Locate every Plasmodium parasite and every leukocyte.
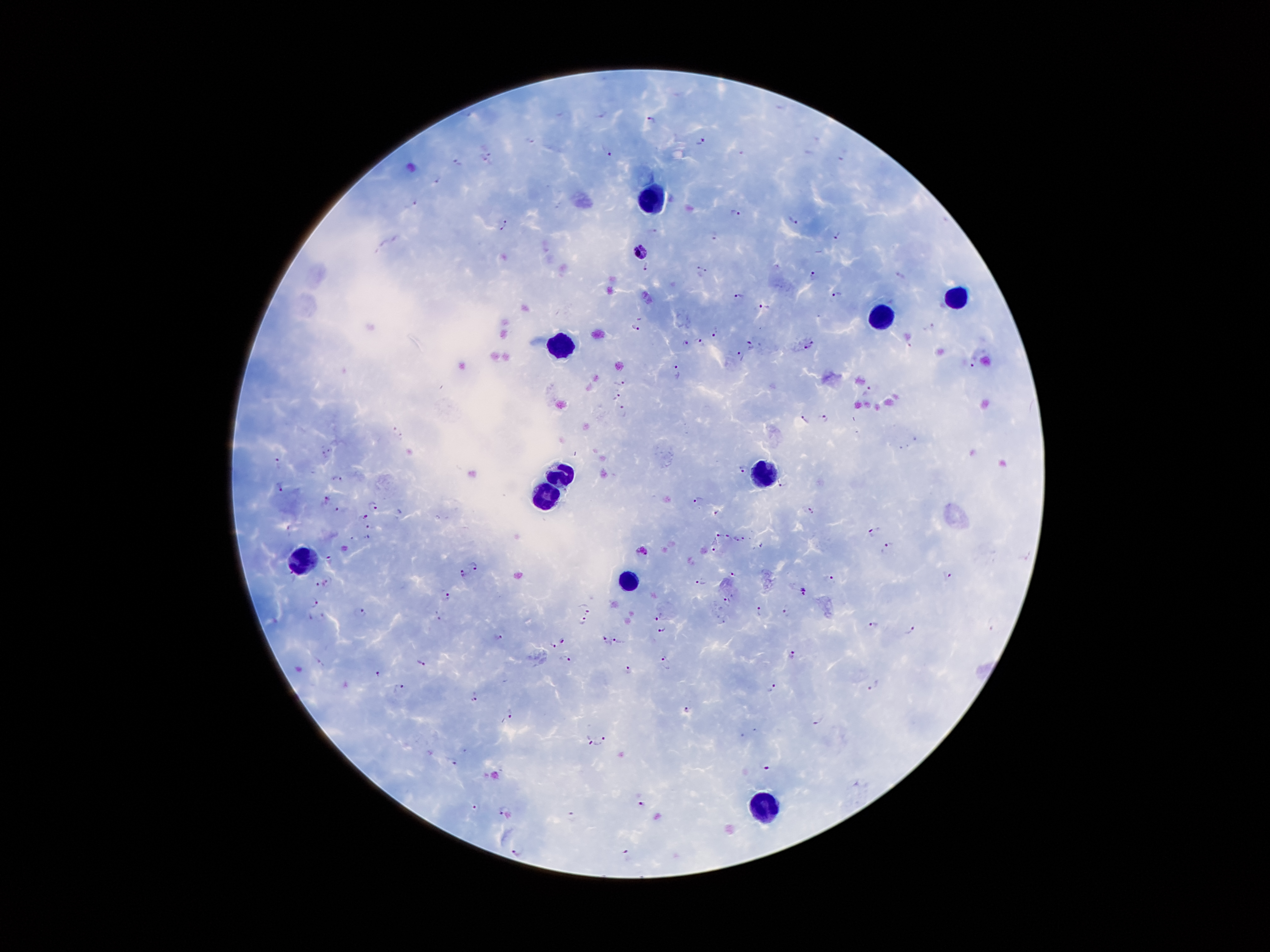
Approximate object centers, in pixels from the top-left corner.
Plasmodium parasites: (x=650, y=119), (x=701, y=140), (x=528, y=141), (x=484, y=150), (x=607, y=151), (x=459, y=161), (x=484, y=164), (x=436, y=175), (x=414, y=200), (x=736, y=213), (x=793, y=220), (x=506, y=222), (x=500, y=228), (x=839, y=234), (x=714, y=236), (x=640, y=253), (x=646, y=267), (x=702, y=268), (x=813, y=274), (x=900, y=275), (x=837, y=293), (x=739, y=294), (x=766, y=306), (x=635, y=327), (x=931, y=327), (x=715, y=330), (x=687, y=339), (x=702, y=341), (x=749, y=342), (x=807, y=345), (x=740, y=356), (x=972, y=362), (x=678, y=369), (x=618, y=382), (x=872, y=386), (x=616, y=397), (x=624, y=411), (x=825, y=418), (x=802, y=419), (x=332, y=449), (x=324, y=454), (x=277, y=463), (x=743, y=469), (x=342, y=480), (x=781, y=483), (x=280, y=485), (x=327, y=499), (x=696, y=499), (x=373, y=505), (x=810, y=509), (x=337, y=510), (x=717, y=514), (x=365, y=516), (x=370, y=526), (x=871, y=532), (x=720, y=534), (x=729, y=536), (x=367, y=537), (x=744, y=537), (x=737, y=539), (x=716, y=544), (x=889, y=547), (x=644, y=549), (x=330, y=559), (x=475, y=565), (x=463, y=573), (x=732, y=573), (x=948, y=576), (x=829, y=580), (x=702, y=581), (x=327, y=582), (x=318, y=584), (x=803, y=592), (x=447, y=595), (x=727, y=600), (x=315, y=602), (x=586, y=608), (x=760, y=610), (x=788, y=611), (x=361, y=613), (x=659, y=616), (x=584, y=620), (x=875, y=624), (x=912, y=628), (x=663, y=629), (x=499, y=635), (x=607, y=639), (x=563, y=640), (x=618, y=640), (x=554, y=644), (x=792, y=656), (x=566, y=659), (x=667, y=662), (x=421, y=663), (x=629, y=669), (x=379, y=673), (x=874, y=684), (x=399, y=685), (x=772, y=688), (x=474, y=695), (x=688, y=710), (x=509, y=713), (x=818, y=721), (x=589, y=740), (x=602, y=740), (x=455, y=762), (x=765, y=766), (x=640, y=804), (x=477, y=806), (x=502, y=810), (x=572, y=816), (x=518, y=851), (x=627, y=856).
Leukocytes: (x=650, y=202), (x=959, y=298), (x=883, y=316), (x=563, y=345), (x=560, y=473), (x=762, y=480), (x=540, y=493), (x=304, y=562), (x=628, y=586), (x=762, y=807).

Image is 1270×952 pixels. Patient malaria status: positive for Plasmodium falciparum. Giemsa-stained preparation. Thick blood smear. 100x magnification. One field from this slide. Smartphone photograph taken through the microscope eyepiece.